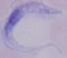
magnification = 1000x
identification = trypanosome
modality = photomicrograph